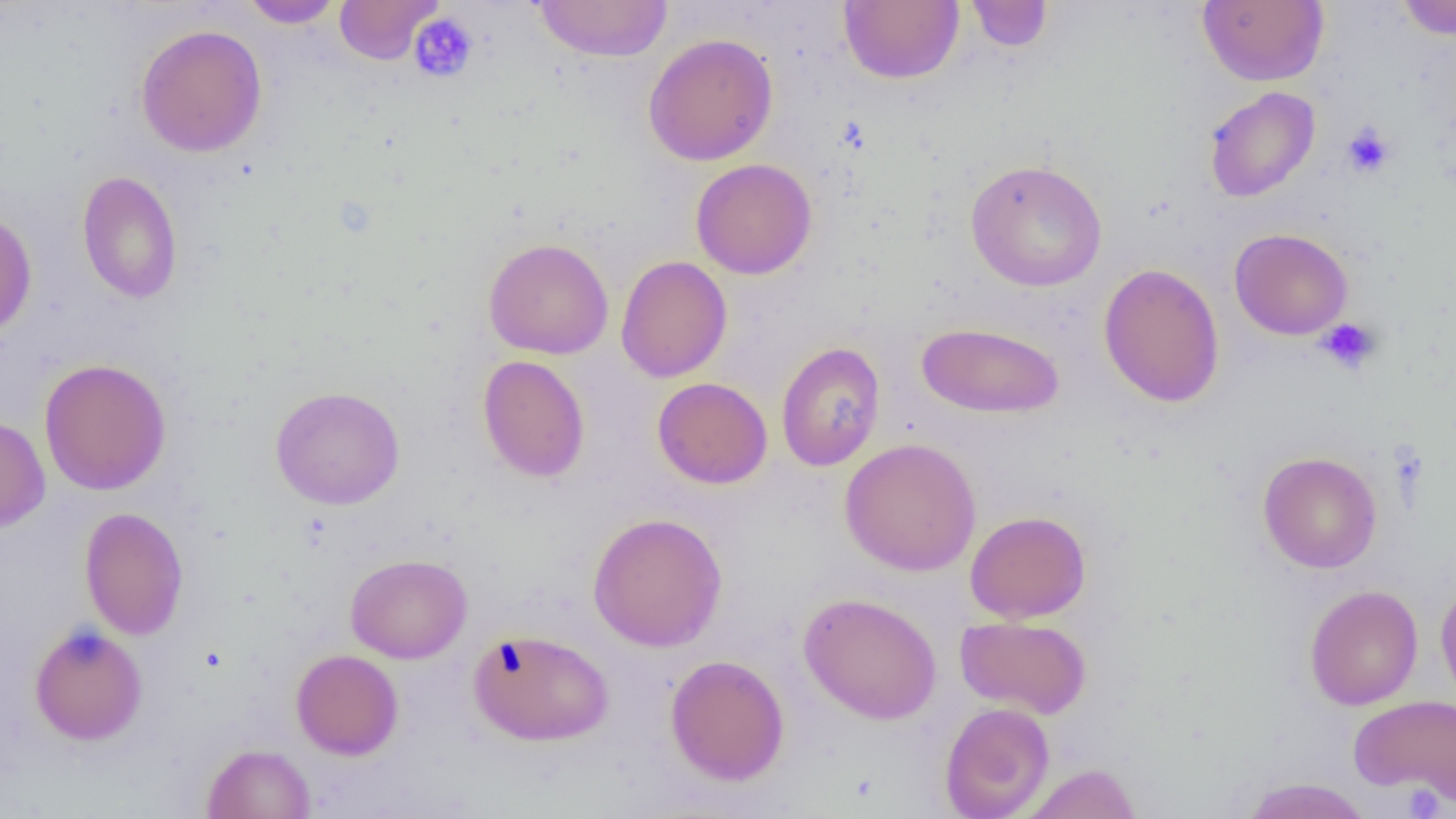

slide-level diagnosis = negative for blood parasites
field of view = single
magnification = 1000x
preparation = thin blood film
modality = light microscopy
platelet locations = approximate bounding boxes as named x1/y1/x2/y2 corners in pixels: (x1=336, y1=1, x2=445, y2=65), (x1=408, y1=13, x2=479, y2=83), (x1=1341, y1=123, x2=1395, y2=178), (x1=1316, y1=318, x2=1381, y2=374), (x1=1401, y1=784, x2=1446, y2=817)
uninfected red blood cell locations = approximate bounding boxes as named x1/y1/x2/y2 corners in pixels: (x1=334, y1=0, x2=443, y2=64), (x1=965, y1=0, x2=1053, y2=52), (x1=1197, y1=0, x2=1328, y2=86), (x1=1395, y1=0, x2=1456, y2=40), (x1=240, y1=1, x2=344, y2=28), (x1=533, y1=1, x2=673, y2=62), (x1=839, y1=1, x2=964, y2=84), (x1=136, y1=23, x2=268, y2=158), (x1=642, y1=32, x2=778, y2=166), (x1=1204, y1=87, x2=1320, y2=203), (x1=691, y1=158, x2=817, y2=279), (x1=965, y1=159, x2=1107, y2=292), (x1=77, y1=170, x2=184, y2=304), (x1=0, y1=208, x2=37, y2=338), (x1=1229, y1=228, x2=1353, y2=340), (x1=483, y1=238, x2=614, y2=360), (x1=616, y1=255, x2=732, y2=383), (x1=1098, y1=263, x2=1224, y2=408), (x1=915, y1=322, x2=1066, y2=419), (x1=776, y1=341, x2=885, y2=472), (x1=477, y1=354, x2=590, y2=482), (x1=39, y1=358, x2=171, y2=495), (x1=652, y1=377, x2=773, y2=489), (x1=270, y1=386, x2=405, y2=509), (x1=0, y1=415, x2=50, y2=532), (x1=839, y1=437, x2=981, y2=577), (x1=1258, y1=451, x2=1382, y2=573), (x1=79, y1=507, x2=189, y2=641), (x1=965, y1=510, x2=1092, y2=623), (x1=587, y1=512, x2=727, y2=652), (x1=345, y1=554, x2=472, y2=663), (x1=1436, y1=578, x2=1456, y2=710), (x1=1304, y1=584, x2=1423, y2=710), (x1=798, y1=592, x2=942, y2=725), (x1=955, y1=615, x2=1092, y2=719), (x1=28, y1=623, x2=147, y2=746), (x1=467, y1=628, x2=614, y2=746), (x1=290, y1=649, x2=404, y2=760), (x1=665, y1=654, x2=790, y2=786), (x1=1349, y1=695, x2=1456, y2=803), (x1=940, y1=701, x2=1054, y2=818), (x1=201, y1=743, x2=316, y2=819), (x1=1022, y1=763, x2=1142, y2=819), (x1=1237, y1=778, x2=1374, y2=819)
image size = 1456×819 pixels